Locate every blood parasite and identify its species.
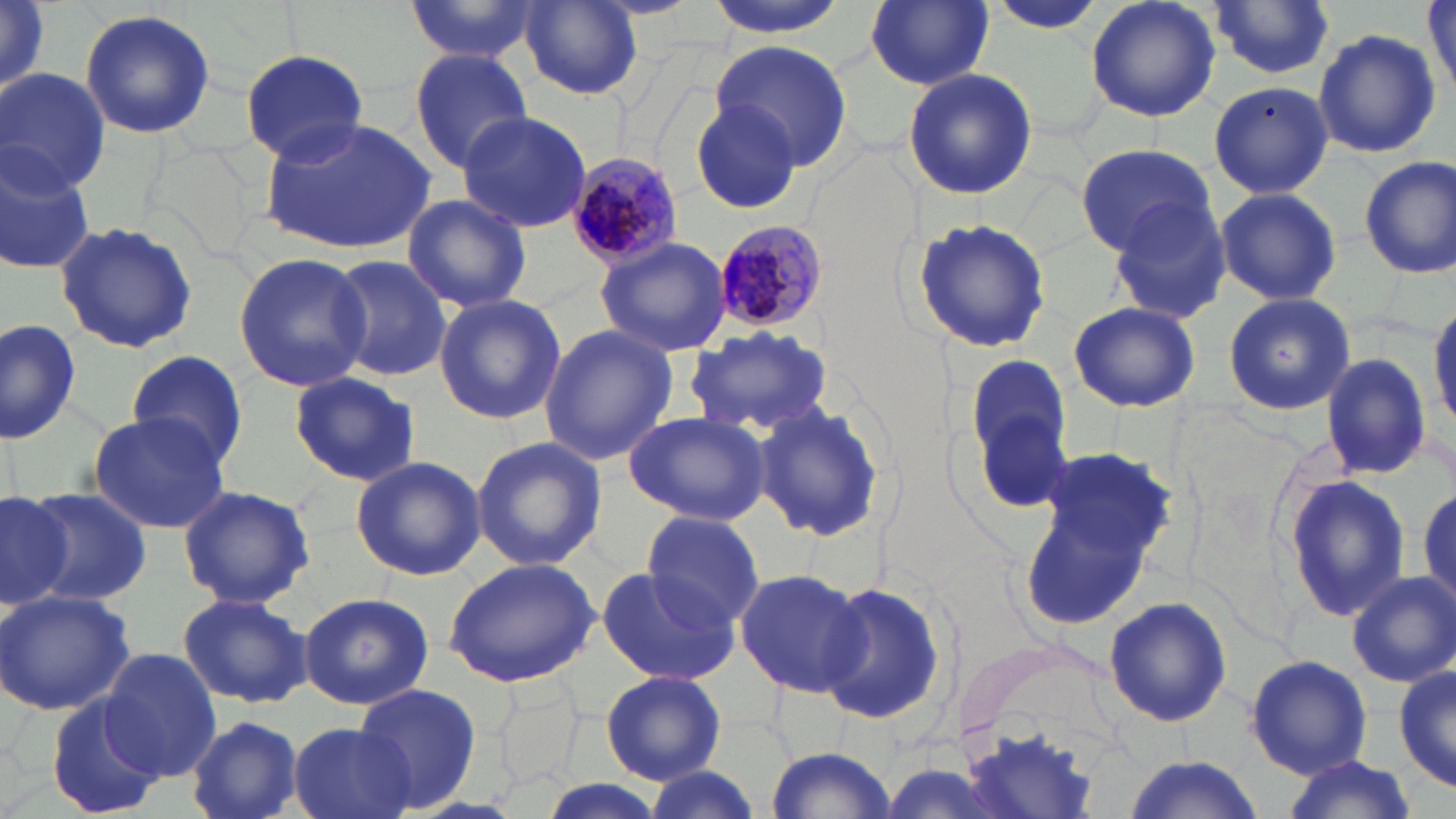
Approximate bounding boxes as [x1, y1, x2, y2] in pixels.
Plasmodium malariae-infected red blood cells: [562, 151, 685, 269], [709, 218, 829, 333].
No Plasmodium falciparum, Plasmodium ovale, Plasmodium vivax, Babesia divergens, or Trypanosoma brucei observed.

Uninfected red blood cell locations: [402, 0, 544, 65], [1086, 0, 1220, 123], [705, 1, 851, 38], [865, 1, 993, 88], [518, 2, 645, 101], [986, 2, 1108, 36], [1208, 2, 1337, 80], [1423, 4, 1456, 93], [79, 10, 218, 140], [1312, 28, 1440, 161], [711, 40, 853, 174], [242, 44, 372, 164], [406, 47, 534, 172], [902, 66, 1037, 201], [0, 68, 110, 195], [1208, 81, 1333, 201], [687, 100, 811, 215], [456, 111, 592, 234], [260, 117, 437, 252], [1073, 142, 1217, 258], [0, 147, 95, 275], [1357, 155, 1456, 279], [1214, 187, 1341, 306], [401, 192, 532, 313], [1106, 199, 1235, 325], [412, 210, 543, 411], [910, 217, 1055, 354], [53, 221, 199, 356], [594, 237, 734, 356], [232, 252, 372, 394], [328, 255, 449, 384], [1222, 292, 1355, 416], [433, 294, 566, 425], [1429, 295, 1456, 437], [1067, 301, 1201, 413], [0, 319, 80, 445], [539, 325, 676, 465], [685, 326, 836, 440], [125, 350, 250, 468], [1319, 352, 1430, 482], [967, 355, 1070, 460], [290, 371, 419, 487], [752, 398, 888, 541], [87, 411, 230, 535], [625, 411, 772, 527], [470, 435, 607, 571], [1020, 445, 1174, 623], [350, 457, 485, 580], [1278, 476, 1415, 622], [176, 483, 316, 609], [24, 485, 153, 611], [0, 488, 76, 606], [640, 511, 764, 633], [443, 558, 602, 686], [594, 565, 739, 686], [733, 567, 869, 697], [1346, 572, 1455, 686], [816, 581, 950, 728], [0, 589, 135, 717], [177, 591, 312, 708], [298, 591, 434, 710], [1103, 596, 1234, 728], [99, 649, 222, 780], [1245, 653, 1372, 777], [1394, 661, 1455, 794], [600, 670, 725, 784], [499, 682, 579, 792], [353, 683, 481, 813], [44, 692, 163, 814], [187, 714, 304, 819], [958, 720, 1100, 817], [290, 722, 413, 819], [765, 745, 898, 818], [1116, 756, 1269, 819], [1278, 758, 1420, 819], [639, 766, 761, 819], [534, 779, 667, 819]. Slide-level diagnosis: Plasmodium malariae. Light microscopy. Image is 1456×819 pixels. 1000x magnification. Single field of view. May-Grünwald-Giemsa stain. Thin blood smear.